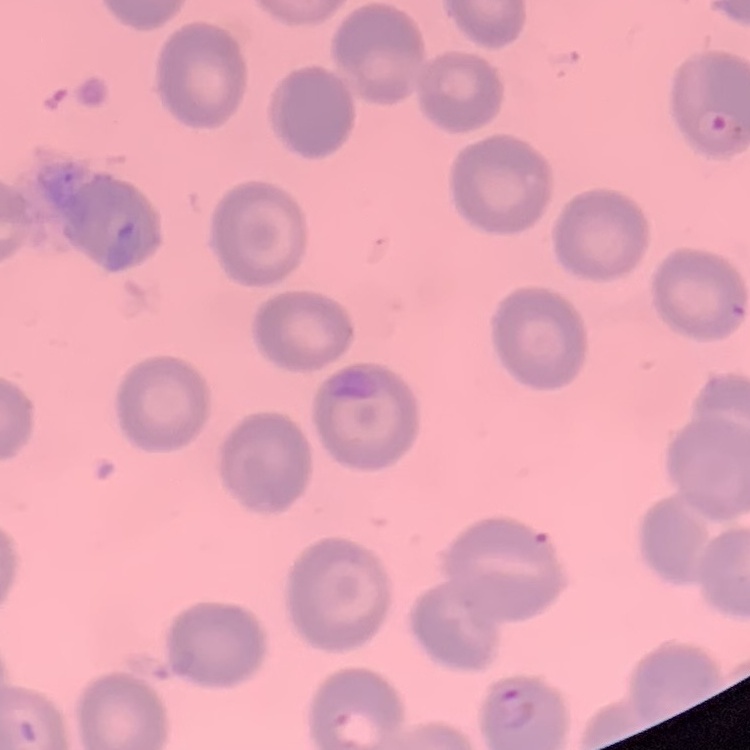 The red blood cells show no rouleaux formation. Thin blood smear. One tile cut from a larger photomicrograph. Stained with either Field's or Giemsa.